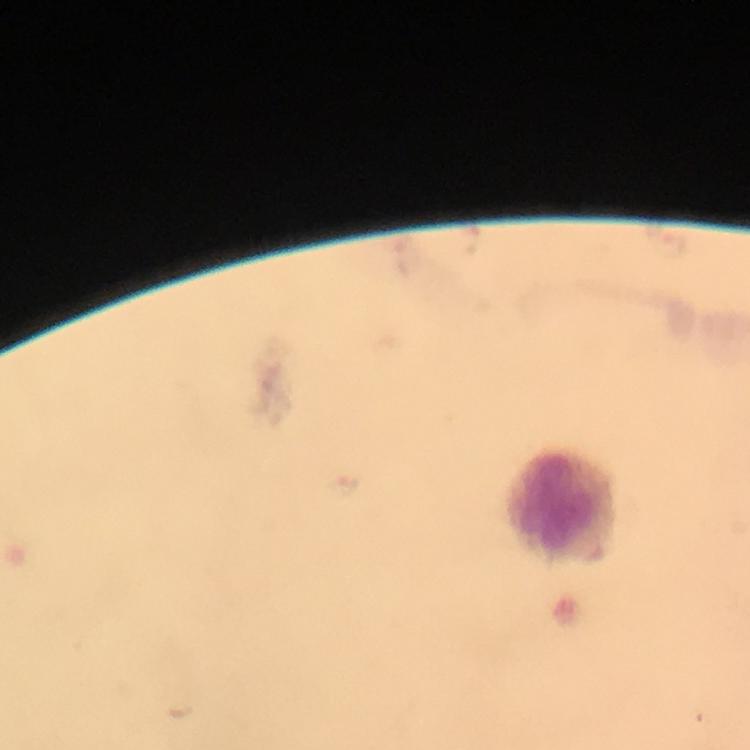

Approximate centers as (x, y) in pixels.
Summary:
  - Leukocyte locations: (567, 507)
  - Magnification: 100x
  - Cropped from: one field of view
  - Context: from a diagnostic examination for malaria
  - Preparation: thick blood smear
  - Stain: Giemsa
  - Immersion oil: used
  - Malaria parasites: none seen
  - Capture: smartphone mounted on the microscope
  - Image size: 750×750 pixels